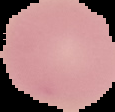
From a thin blood smear. Result: no Plasmodium parasites seen. Segmented cell region on a black background. Image is 115×112 pixels.